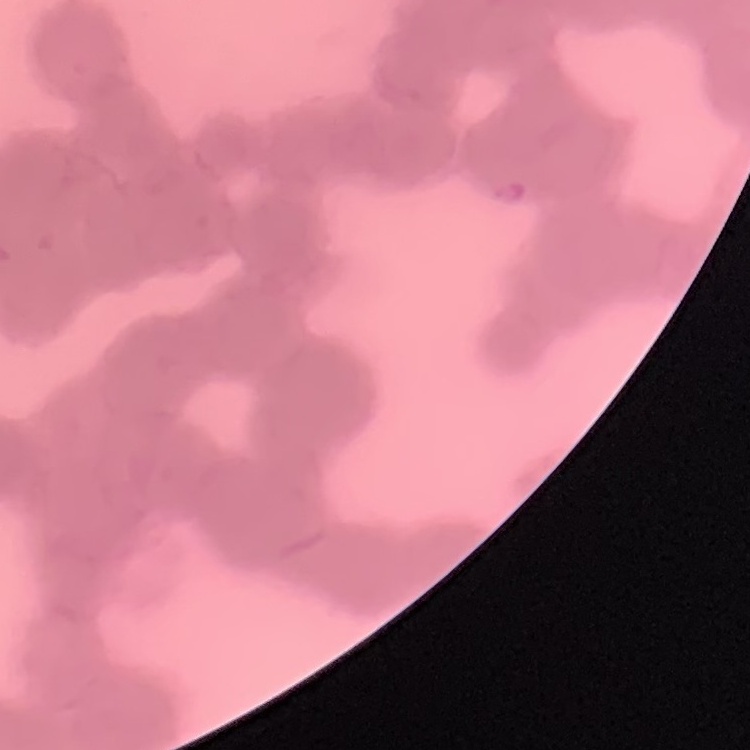
The erythrocytes show rouleaux formation. Field's or Giemsa stain. Square crop of a larger photomicrograph. Thin blood film.